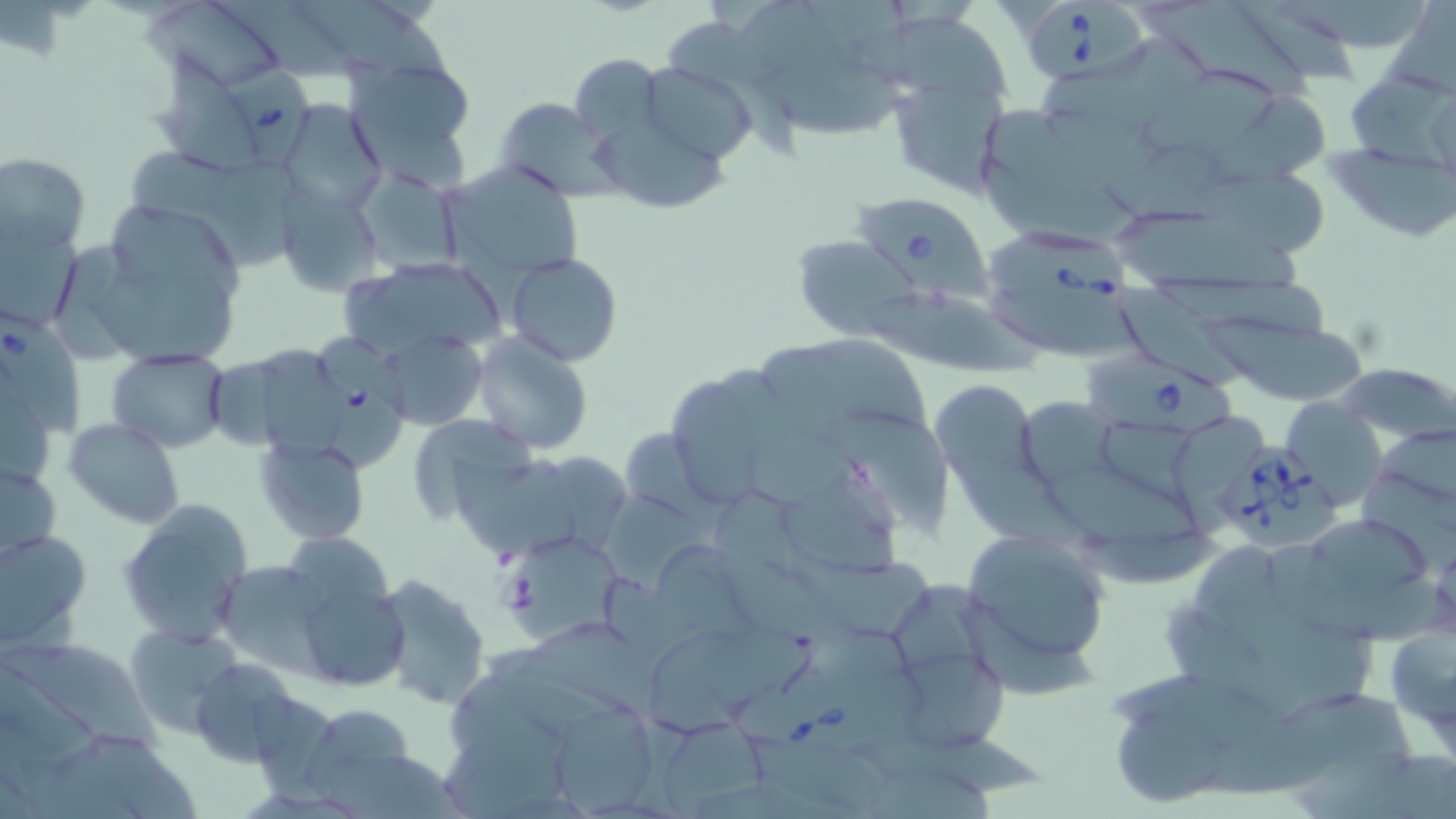

slide-level diagnosis = Babesia divergens
preparation = thin blood smear
field of view = one of a larger specimen
modality = light microscopy
Babesia divergens-infected red blood cell locations = approximate bounding boxes as (x1, y1, x2, y2) in pixels: (1026, 1, 1150, 82), (224, 60, 306, 168), (854, 195, 991, 297), (987, 224, 1137, 310), (0, 314, 89, 441), (315, 335, 406, 465), (1082, 353, 1238, 436), (1211, 439, 1343, 551), (732, 676, 913, 767)
stain = May-Grünwald-Giemsa
platelet locations = approximate bounding boxes as (x1, y1, x2, y2) in pixels: (499, 567, 540, 612)
magnification = 1000x
uninfected red blood cell locations = approximate bounding boxes as (x1, y1, x2, y2) in pixels: (139, 0, 285, 84), (217, 0, 353, 83), (297, 0, 457, 89), (728, 0, 824, 90), (805, 0, 916, 75), (1139, 0, 1313, 106), (1240, 0, 1364, 89), (1287, 0, 1435, 51), (1384, 1, 1456, 100), (848, 12, 1023, 107), (661, 15, 765, 88), (1041, 36, 1213, 121), (349, 53, 478, 178), (149, 54, 261, 178), (569, 54, 666, 151), (768, 58, 903, 133), (644, 62, 757, 164), (1146, 65, 1283, 155), (1346, 75, 1456, 168), (893, 90, 1013, 193), (1208, 94, 1334, 184), (493, 97, 620, 197), (280, 99, 386, 213), (1046, 104, 1167, 181), (985, 108, 1118, 199), (591, 121, 730, 210), (1107, 142, 1248, 230), (126, 149, 301, 272), (1322, 152, 1456, 240), (1, 153, 91, 256), (978, 154, 1148, 252), (437, 161, 586, 286), (1186, 166, 1336, 257), (352, 168, 464, 276), (276, 186, 385, 298), (79, 200, 254, 373), (1116, 209, 1309, 291), (1, 220, 81, 332), (795, 235, 914, 340), (505, 252, 625, 368), (348, 255, 508, 360), (1145, 269, 1337, 345), (866, 283, 1043, 370), (1119, 286, 1254, 392), (983, 288, 1144, 360), (1197, 307, 1367, 402), (378, 329, 487, 430), (472, 334, 595, 456), (817, 338, 931, 433), (259, 345, 343, 466), (760, 345, 858, 452), (106, 346, 230, 452), (209, 359, 285, 450), (1338, 363, 1456, 445), (666, 377, 765, 507), (932, 379, 1043, 498), (1281, 397, 1389, 514), (1015, 398, 1120, 488), (837, 402, 956, 544), (403, 411, 539, 526), (1179, 413, 1267, 531), (1100, 415, 1195, 522), (63, 417, 184, 529), (1375, 423, 1456, 499), (749, 426, 891, 522), (619, 429, 707, 516), (253, 434, 370, 546), (955, 450, 1092, 553), (453, 456, 581, 556), (1, 459, 62, 560), (544, 460, 631, 548), (1044, 464, 1199, 551), (1357, 470, 1456, 580), (783, 483, 897, 571), (710, 485, 807, 568), (595, 494, 716, 592), (118, 502, 253, 646), (1309, 517, 1435, 599), (1080, 522, 1228, 588), (0, 529, 92, 649), (281, 530, 395, 624), (962, 531, 1111, 673), (507, 534, 627, 642), (1190, 540, 1296, 640), (661, 543, 768, 643), (792, 549, 933, 643), (715, 550, 826, 640), (216, 561, 330, 673), (370, 573, 490, 709), (293, 579, 408, 693), (894, 586, 988, 698), (955, 598, 1099, 704), (1161, 600, 1303, 720), (1246, 606, 1374, 720), (1381, 614, 1456, 751), (122, 622, 244, 737), (782, 623, 923, 704), (514, 626, 662, 725), (648, 628, 815, 739), (8, 643, 166, 751), (900, 656, 1011, 756), (191, 657, 300, 766), (1108, 665, 1288, 755), (444, 668, 568, 765), (1276, 695, 1403, 763), (552, 702, 654, 814), (304, 705, 416, 801), (1116, 713, 1230, 803), (661, 718, 768, 818), (851, 726, 1042, 798), (1211, 728, 1360, 801), (67, 729, 200, 819), (436, 731, 576, 819), (752, 736, 895, 812), (1293, 752, 1420, 819), (1381, 752, 1456, 819), (326, 755, 474, 819), (868, 764, 1005, 819)
image size = 1456×819 pixels